Identify the parasite.
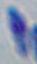
Toxoplasma gondii.

Micrograph. Captured at 1000x magnification.